Assess this cell for malaria.
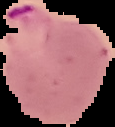

Parasitized.

image_type: segmented cell region on a black background
image_size: 115×127 pixels
preparation: thin blood film